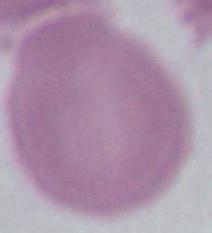 Photomicrograph. A red blood cell is shown. Captured at 1000x magnification.